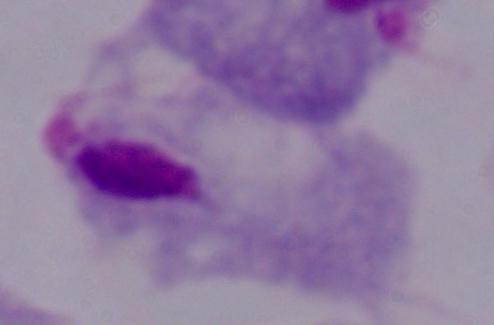 A trichomonad is shown. 1000x magnification. Photomicrograph.